Locate every leukocyte (white blood cell).
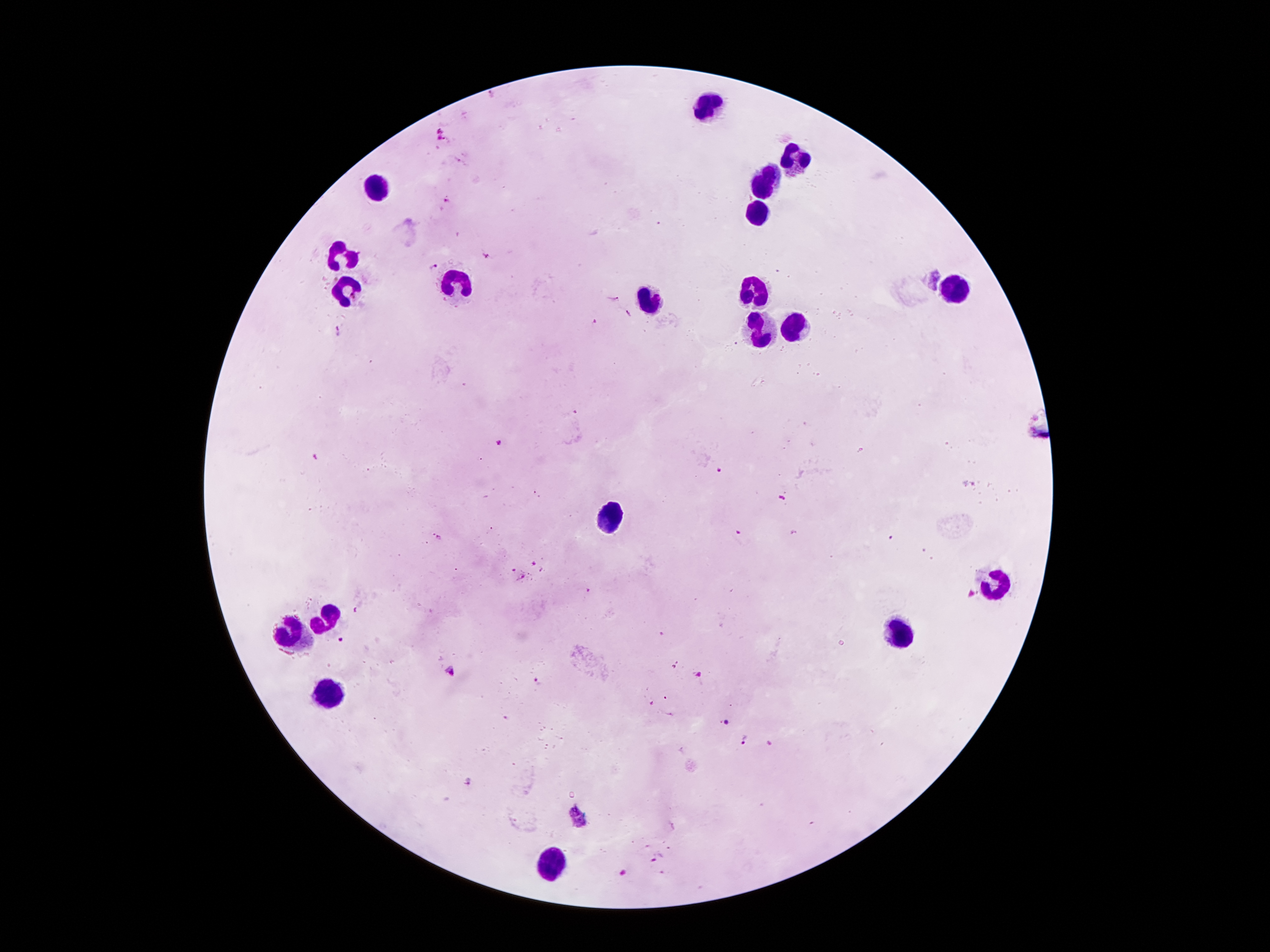

Approximate object centers, in pixels from the top-left corner.
Leukocytes: (x=708, y=105), (x=792, y=157), (x=766, y=176), (x=377, y=186), (x=753, y=215), (x=340, y=255), (x=459, y=283), (x=348, y=289), (x=753, y=291), (x=952, y=291), (x=650, y=297), (x=755, y=328), (x=792, y=328), (x=608, y=520), (x=994, y=580), (x=327, y=617), (x=900, y=627), (x=296, y=632), (x=327, y=695), (x=550, y=861).

Plasmodium parasite locations: (x=490, y=92), (x=439, y=129), (x=439, y=139), (x=447, y=202), (x=486, y=257), (x=433, y=265), (x=931, y=278), (x=615, y=299), (x=627, y=314), (x=595, y=322), (x=339, y=330), (x=575, y=413), (x=499, y=443), (x=314, y=457), (x=718, y=469), (x=781, y=500), (x=437, y=536), (x=533, y=564), (x=512, y=570), (x=522, y=575), (x=587, y=589), (x=356, y=610), (x=339, y=640), (x=673, y=666), (x=449, y=670), (x=699, y=676), (x=539, y=683), (x=652, y=703), (x=727, y=724), (x=745, y=739), (x=769, y=743), (x=469, y=780), (x=573, y=807), (x=584, y=825), (x=655, y=859), (x=623, y=873). Patient malaria status: infected with Plasmodium falciparum. Thick blood smear. Image is 1270×952 pixels. Smartphone photograph taken through the microscope eyepiece. Single field of view. Giemsa-stained preparation. 100x magnification.